Assess the morphology of the erythrocytes.
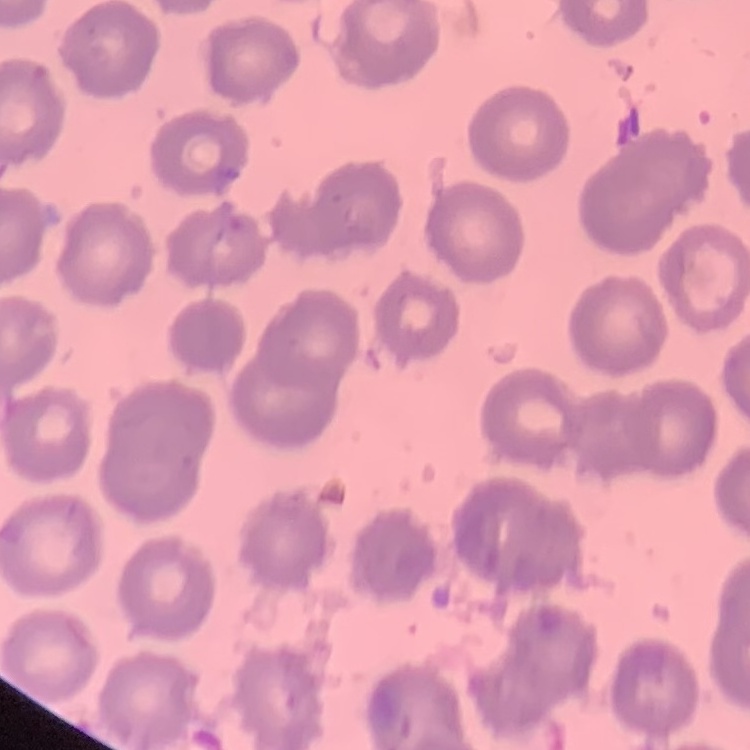

No rouleaux formation.

Thin blood smear. Field's or Giemsa stain. Square crop of a larger photomicrograph.